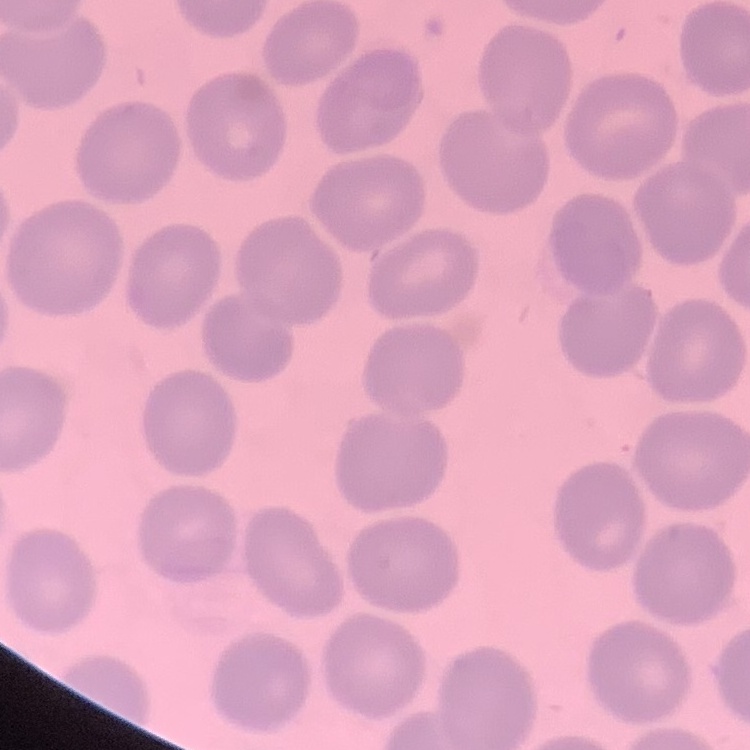
The red blood cells show no rouleaux formation. Thin peripheral smear. Field's or Giemsa stain. One tile cut from a larger photomicrograph.